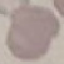
Malaria status: uninfected. Photographed with a smartphone camera at the microscope eyepiece. Automatically extracted cell patch, resized to 64 × 64 pixels. Giemsa-stained preparation. Thin smear of blood.